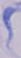
Summary:
  - Modality: micrograph
  - Magnification: 1000x
  - Identification: trypanosome